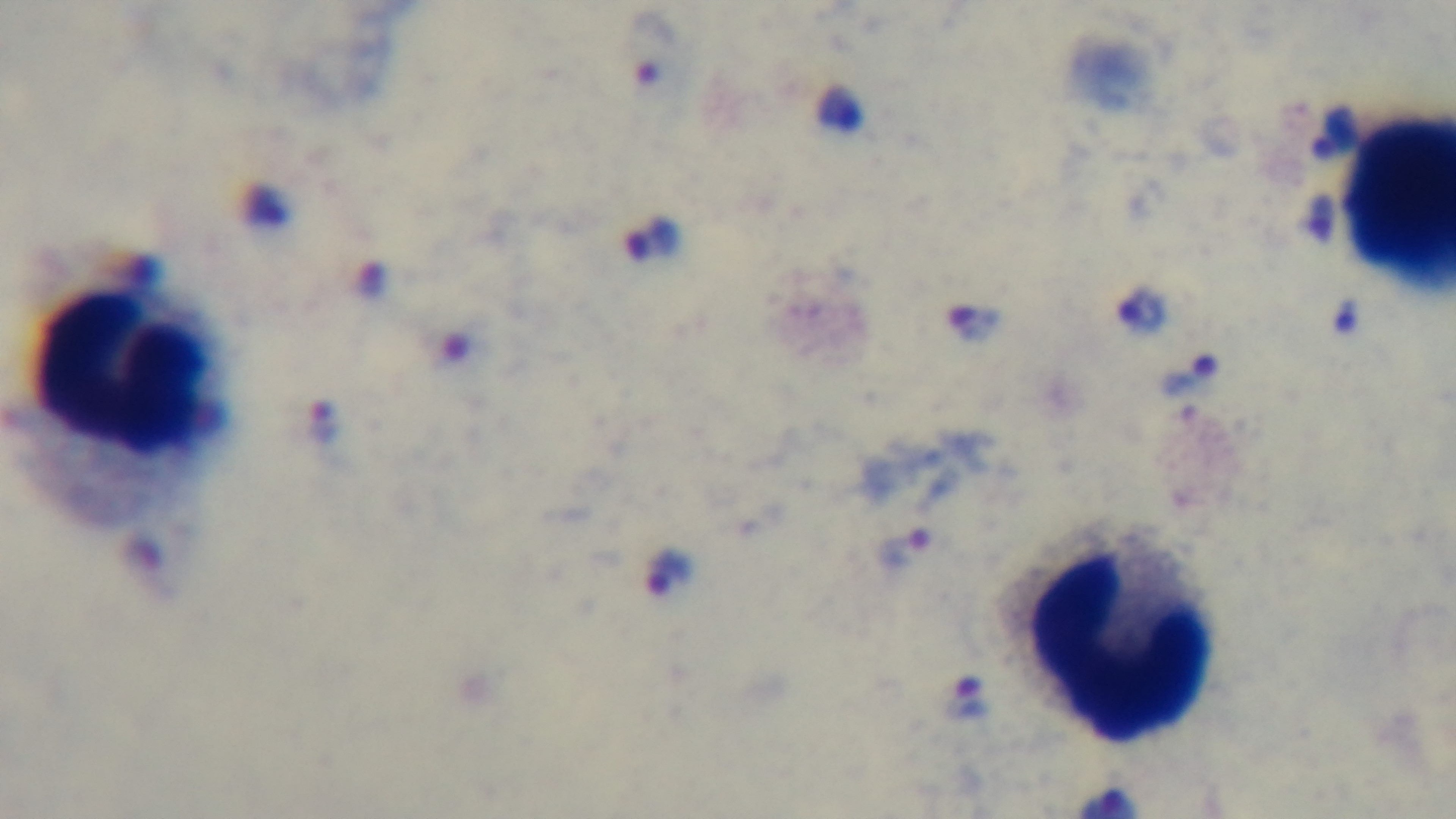

preparation = thick smear
modality = light microscopy
malaria status = infected
stain = Giemsa
field of view = single
objective = 100x oil immersion
capture = mounted 4K digital camera